Report the malaria status of this cell.
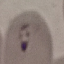
Parasitized.

Summary:
  - Capture: smartphone through the microscope eyepiece
  - Preparation: thin blood film
  - Stain: Giemsa
  - Image type: automatically extracted cell patch, resized to 64 × 64 pixels